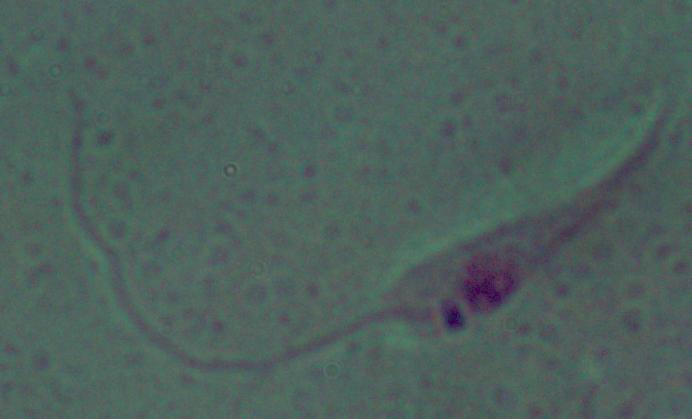 1000x magnification. A Leishmania parasite is seen. Micrograph.